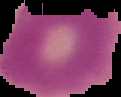

Malaria status: uninfected. From a thin blood film. Cell region segmented out of the field of view; the surrounding area is masked to black. Image is 121×97 pixels.